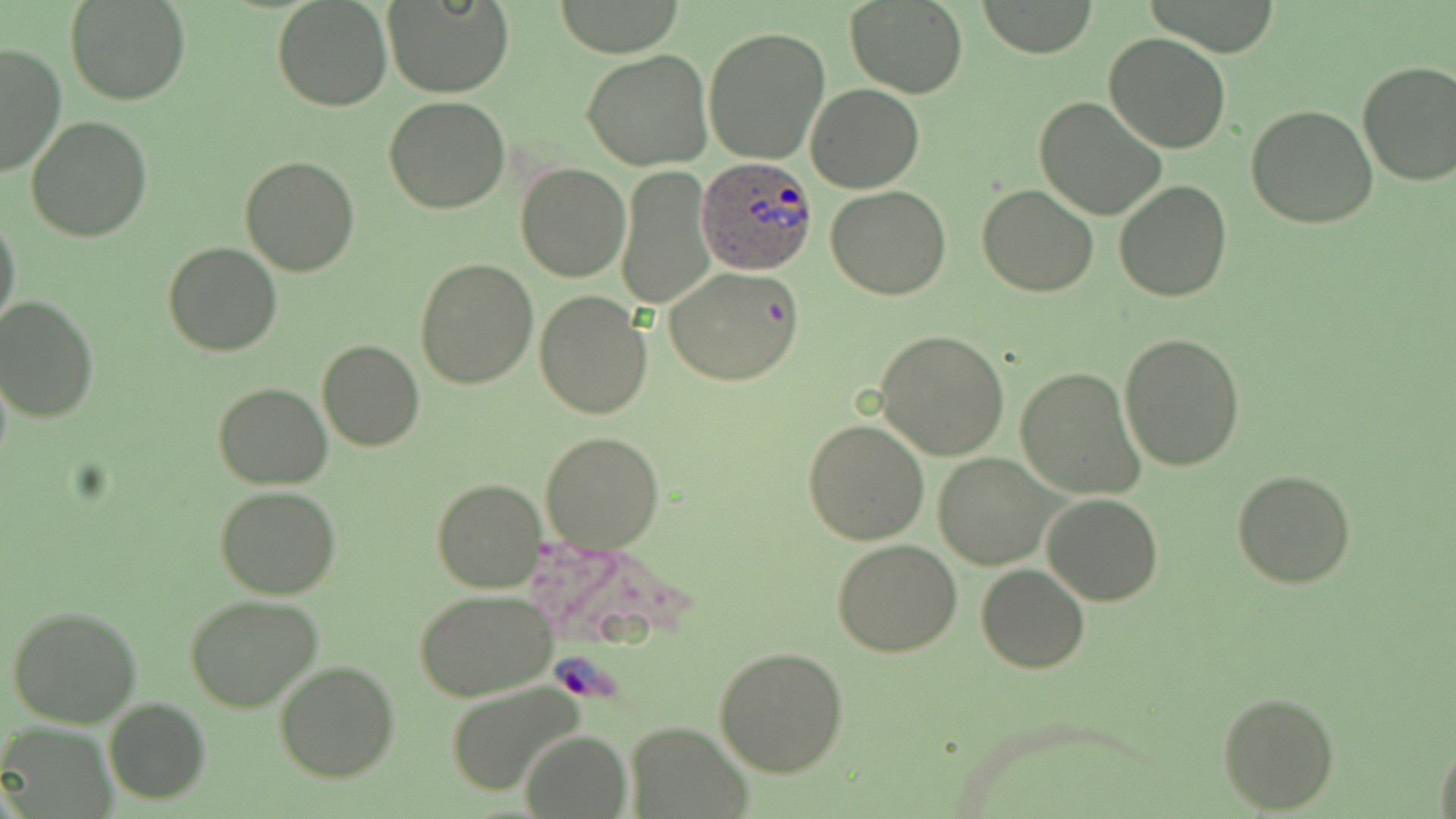
slide-level diagnosis = Plasmodium ovale
field of view = one of a larger specimen
uninfected red blood cell locations = approximate bounding boxes as [x1, y1, x2, y2] in pixels: [272, 0, 392, 111], [385, 0, 511, 98], [844, 0, 968, 97], [978, 0, 1099, 57], [66, 1, 193, 105], [554, 1, 685, 56], [703, 25, 831, 165], [1103, 33, 1232, 153], [0, 41, 67, 178], [582, 52, 714, 170], [1356, 60, 1456, 187], [807, 85, 924, 192], [1034, 95, 1166, 222], [384, 97, 511, 215], [1246, 105, 1378, 228], [26, 116, 154, 242], [240, 156, 359, 276], [515, 162, 630, 282], [617, 166, 714, 309], [1113, 179, 1232, 301], [977, 184, 1100, 297], [826, 185, 951, 299], [0, 214, 21, 340], [162, 241, 283, 358], [415, 257, 539, 389], [664, 268, 803, 386], [534, 290, 653, 418], [1, 295, 101, 423], [875, 330, 1009, 461], [1119, 332, 1247, 471], [318, 341, 423, 451], [1015, 366, 1145, 499], [213, 382, 332, 489], [802, 418, 930, 545], [540, 430, 667, 554], [933, 453, 1056, 568], [1232, 469, 1358, 588], [431, 477, 547, 594], [215, 487, 342, 600], [1043, 493, 1163, 605], [832, 539, 964, 657], [976, 563, 1089, 673], [413, 588, 558, 702], [185, 596, 324, 714], [7, 604, 142, 728], [715, 644, 849, 776], [275, 661, 399, 782], [441, 681, 590, 799], [1218, 689, 1338, 812], [103, 697, 210, 804], [624, 722, 750, 817], [0, 723, 118, 818], [522, 729, 630, 817], [1434, 730, 1455, 819]
stain = May-Grünwald-Giemsa
modality = light microscopy
Plasmodium ovale-infected red blood cell locations = approximate bounding boxes as [x1, y1, x2, y2] in pixels: [698, 156, 818, 277]
magnification = 1000x
preparation = thin blood film
image size = 1456×819 pixels